Give the extent of all Plasmodium falciparum-infected red blood cells.
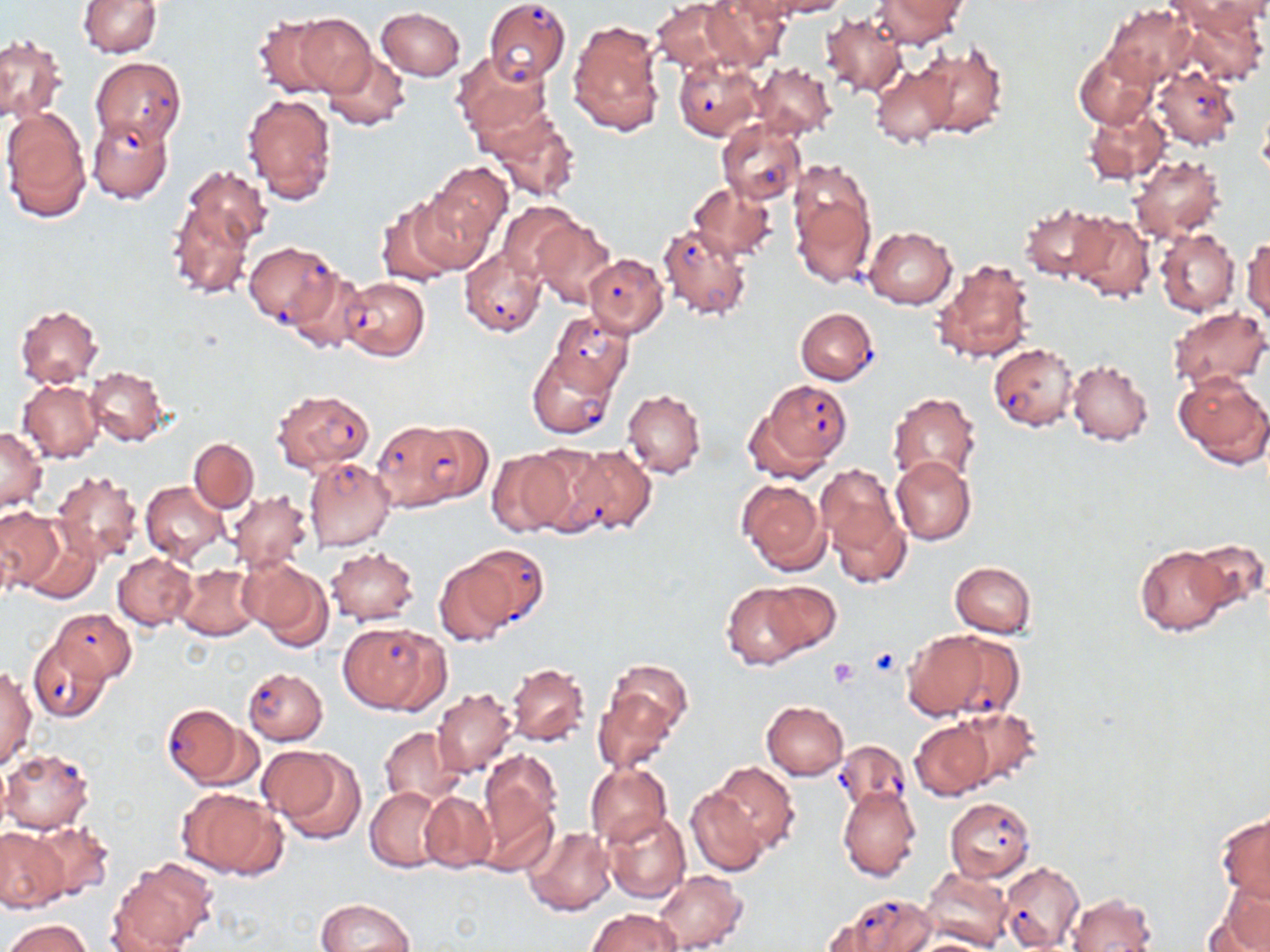
Approximate bounding boxes as (x1, y1, x2, y2) in pixels.
Plasmodium falciparum-infected red blood cells: (484, 0, 571, 87), (92, 56, 185, 147), (674, 56, 763, 141), (1152, 66, 1241, 150), (717, 121, 805, 205), (657, 222, 752, 320), (244, 242, 336, 329), (459, 247, 546, 337), (583, 253, 668, 337), (342, 276, 429, 361), (795, 307, 878, 384), (550, 311, 633, 395), (989, 343, 1080, 431), (528, 351, 616, 440), (758, 380, 851, 469), (272, 388, 373, 472), (370, 419, 467, 513), (412, 421, 492, 505), (560, 443, 656, 537), (304, 457, 397, 552), (458, 544, 550, 629), (53, 609, 136, 681), (339, 621, 446, 714), (905, 629, 1006, 720), (27, 636, 110, 722), (243, 668, 328, 745), (163, 706, 249, 788), (834, 739, 911, 817), (1, 749, 95, 833), (944, 797, 1034, 881), (1000, 861, 1085, 951), (833, 895, 936, 952).

slide-level diagnosis = Plasmodium falciparum
platelet locations = approximate bounding boxes as (x1, y1, x2, y2) in pixels: (828, 657, 859, 687)
uninfected red blood cell locations = approximate bounding boxes as (x1, y1, x2, y2) in pixels: (77, 0, 160, 57), (651, 0, 747, 71), (770, 0, 847, 18), (1171, 0, 1268, 84), (701, 1, 791, 69), (871, 1, 965, 47), (1103, 5, 1196, 88), (376, 7, 466, 80), (819, 13, 908, 99), (287, 14, 377, 97), (569, 21, 665, 136), (0, 35, 64, 124), (918, 42, 1007, 140), (318, 51, 411, 132), (1075, 51, 1155, 128), (453, 53, 551, 139), (869, 59, 959, 148), (753, 62, 837, 138), (242, 91, 339, 206), (1084, 105, 1170, 184), (2, 107, 92, 221), (486, 109, 580, 203), (87, 116, 172, 204), (1130, 154, 1225, 244), (430, 161, 512, 241), (182, 166, 272, 248), (789, 181, 875, 287), (688, 182, 777, 260), (406, 189, 498, 275), (166, 201, 255, 300), (377, 201, 463, 288), (498, 202, 584, 281), (1019, 203, 1108, 281), (1068, 212, 1154, 303), (531, 219, 616, 307), (863, 227, 956, 309), (1156, 228, 1239, 318), (1244, 237, 1270, 323), (930, 257, 1035, 365), (284, 269, 368, 355), (14, 304, 103, 388), (1166, 306, 1269, 390), (1067, 359, 1154, 445), (85, 367, 168, 446), (1174, 370, 1270, 467), (18, 381, 103, 462), (623, 388, 705, 478), (887, 392, 982, 486), (0, 426, 48, 511), (188, 439, 259, 512), (489, 446, 579, 536), (891, 456, 975, 546), (817, 465, 906, 574), (52, 470, 144, 566), (737, 478, 828, 574), (140, 481, 228, 563), (227, 490, 314, 574), (0, 506, 63, 592), (17, 526, 102, 605), (1183, 537, 1270, 616), (1133, 545, 1232, 636), (326, 546, 420, 625), (113, 552, 197, 630), (433, 556, 515, 646), (242, 558, 332, 649), (950, 561, 1036, 637), (174, 564, 261, 642), (760, 581, 842, 654), (721, 582, 812, 669), (604, 658, 692, 751), (507, 662, 590, 746), (0, 667, 36, 768), (594, 688, 676, 772), (433, 689, 516, 777), (761, 701, 848, 779), (955, 707, 1042, 788), (911, 718, 993, 799), (379, 725, 465, 805), (261, 746, 365, 844), (480, 749, 562, 840), (709, 761, 800, 854), (584, 765, 672, 846), (177, 786, 284, 880), (365, 786, 446, 872), (685, 786, 768, 876), (838, 787, 921, 882), (418, 791, 497, 874), (475, 793, 559, 878), (602, 811, 691, 903), (1216, 813, 1270, 903), (30, 821, 115, 902), (0, 826, 68, 912), (524, 826, 614, 916), (109, 858, 217, 951), (920, 865, 1012, 950), (655, 870, 747, 951), (1212, 878, 1270, 951), (1066, 893, 1158, 951), (315, 898, 414, 952), (587, 907, 681, 951), (5, 919, 91, 952)
magnification = 1000x
modality = light microscopy
preparation = thin blood smear
stain = May-Grünwald-Giemsa
image size = 1270×952 pixels
field of view = one of a larger specimen